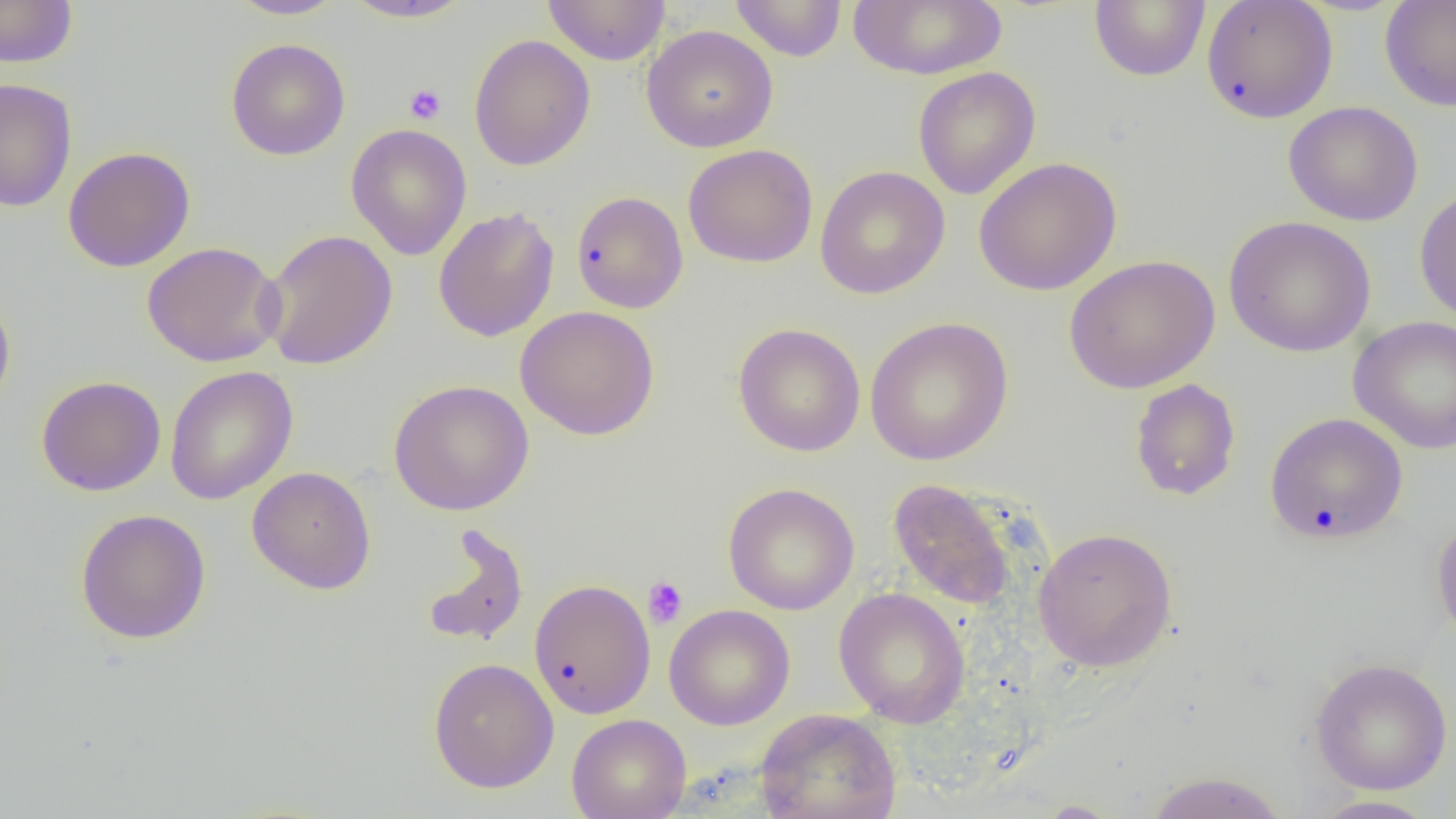

Summary:
  - Coordinate format: approximate bounding boxes as named x1/y1/x2/y2 corners in pixels
  - Uninfected red blood cell locations: (x1=0, y1=0, x2=78, y2=68), (x1=228, y1=0, x2=345, y2=20), (x1=341, y1=0, x2=475, y2=23), (x1=542, y1=0, x2=671, y2=66), (x1=730, y1=0, x2=847, y2=61), (x1=847, y1=0, x2=1007, y2=80), (x1=1089, y1=0, x2=1210, y2=82), (x1=1379, y1=0, x2=1456, y2=112), (x1=1201, y1=1, x2=1338, y2=124), (x1=641, y1=25, x2=778, y2=152), (x1=468, y1=34, x2=595, y2=171), (x1=225, y1=38, x2=351, y2=161), (x1=913, y1=66, x2=1041, y2=200), (x1=0, y1=79, x2=78, y2=213), (x1=1283, y1=101, x2=1423, y2=226), (x1=346, y1=123, x2=472, y2=261), (x1=682, y1=143, x2=818, y2=268), (x1=62, y1=146, x2=196, y2=272), (x1=973, y1=157, x2=1122, y2=296), (x1=814, y1=165, x2=950, y2=299), (x1=1414, y1=186, x2=1456, y2=325), (x1=571, y1=191, x2=688, y2=314), (x1=432, y1=207, x2=560, y2=342), (x1=1223, y1=216, x2=1376, y2=357), (x1=260, y1=229, x2=398, y2=370), (x1=141, y1=241, x2=285, y2=367), (x1=1064, y1=254, x2=1220, y2=393), (x1=0, y1=287, x2=16, y2=417), (x1=515, y1=305, x2=660, y2=441), (x1=865, y1=316, x2=1014, y2=466), (x1=1348, y1=316, x2=1456, y2=454), (x1=733, y1=323, x2=865, y2=456), (x1=164, y1=366, x2=299, y2=504), (x1=36, y1=375, x2=166, y2=496), (x1=1130, y1=378, x2=1241, y2=501), (x1=388, y1=379, x2=534, y2=516), (x1=1265, y1=412, x2=1408, y2=544), (x1=247, y1=466, x2=376, y2=595), (x1=887, y1=478, x2=1016, y2=609), (x1=722, y1=482, x2=860, y2=614), (x1=75, y1=509, x2=211, y2=644), (x1=1431, y1=515, x2=1456, y2=649), (x1=422, y1=525, x2=529, y2=649), (x1=1033, y1=526, x2=1178, y2=672), (x1=529, y1=578, x2=656, y2=719), (x1=833, y1=587, x2=971, y2=728), (x1=664, y1=604, x2=795, y2=730), (x1=428, y1=657, x2=559, y2=793), (x1=1310, y1=658, x2=1454, y2=795), (x1=754, y1=708, x2=902, y2=819), (x1=566, y1=713, x2=691, y2=819), (x1=1142, y1=770, x2=1290, y2=819), (x1=1307, y1=795, x2=1441, y2=818), (x1=1034, y1=800, x2=1125, y2=818)
  - Platelet locations: (x1=404, y1=83, x2=446, y2=124), (x1=642, y1=576, x2=688, y2=629)
  - Slide-level diagnosis: no evidence of blood parasites
  - Magnification: 1000x
  - Image size: 1456×819 pixels
  - Field of view: one of a larger specimen
  - Preparation: thin blood film
  - Modality: light microscopy